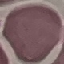
malaria status = uninfected
stain = Giemsa
capture = smartphone camera at the microscope eyepiece
image type = automatically extracted cell patch, resized to 64 × 64 pixels
preparation = thin blood film